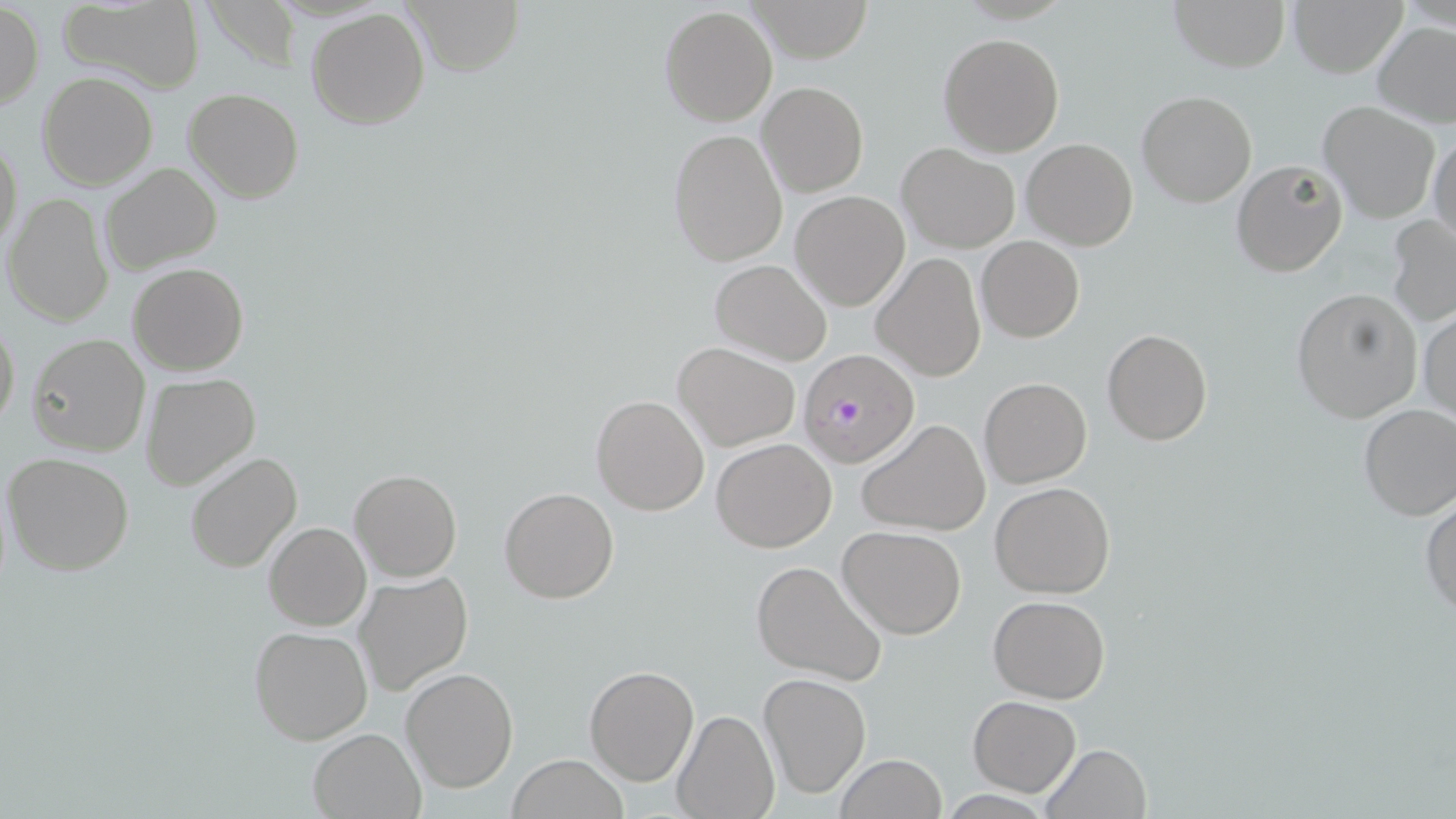

Summary:
  - Coordinate format: approximate bounding boxes as (x1,y1)-(x2,y2) corner pairs in pixels
  - Plasmodium falciparum-infected red blood cell locations: (797,348)-(921,468)
  - Uninfected red blood cell locations: (58,0)-(207,91), (402,0)-(522,77), (743,0)-(876,62), (1167,0)-(1290,73), (1286,0)-(1409,76), (1,3)-(42,108), (660,5)-(779,127), (306,7)-(430,130), (1373,20)-(1456,127), (938,32)-(1064,157), (39,72)-(156,190), (757,82)-(868,197), (184,88)-(304,204), (1136,89)-(1257,208), (1318,101)-(1440,225), (667,127)-(787,267), (0,133)-(23,255), (1429,136)-(1456,249), (1022,138)-(1137,249), (896,141)-(1020,252), (1231,159)-(1348,278), (99,163)-(222,277), (791,190)-(910,311), (4,193)-(114,327), (1386,214)-(1456,327), (976,236)-(1084,342), (872,253)-(986,382), (708,258)-(833,367), (127,262)-(249,375), (1291,286)-(1423,423), (1417,308)-(1455,422), (0,313)-(20,434), (1101,328)-(1214,446), (29,334)-(151,456), (672,340)-(800,450), (140,373)-(262,492), (978,376)-(1092,488), (590,394)-(710,516), (1357,402)-(1456,522), (856,418)-(992,537), (710,438)-(837,552), (184,452)-(302,574), (3,453)-(134,576), (350,468)-(462,583), (989,481)-(1115,599), (500,487)-(619,604), (1421,496)-(1456,619), (264,522)-(371,631), (837,526)-(966,639), (749,559)-(888,686), (353,572)-(473,696), (989,596)-(1111,703), (248,625)-(373,745), (584,665)-(699,785), (401,668)-(519,794), (759,672)-(871,798), (967,695)-(1081,796), (672,709)-(778,819), (308,727)-(426,818), (1040,744)-(1153,819), (832,753)-(948,819), (508,756)-(627,818)
  - Slide-level diagnosis: Plasmodium falciparum
  - Field of view: one of a larger specimen
  - Preparation: thin blood film
  - Stain: May-Grünwald-Giemsa
  - Image size: 1456×819 pixels
  - Modality: light microscopy
  - Magnification: 1000x